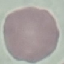

result = no malaria parasites seen
stain = Giemsa
capture = smartphone camera at the microscope eyepiece
image type = automatically extracted cell patch, resized to 64 × 64 pixels
preparation = thin smear